Assess this cell for malaria.
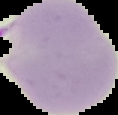

It is parasitized.

Segmented cell region on a black background. Image is 118×115 pixels. From a thin blood film.